Give the extent of all Plasmodium falciparum-infected red blood cells.
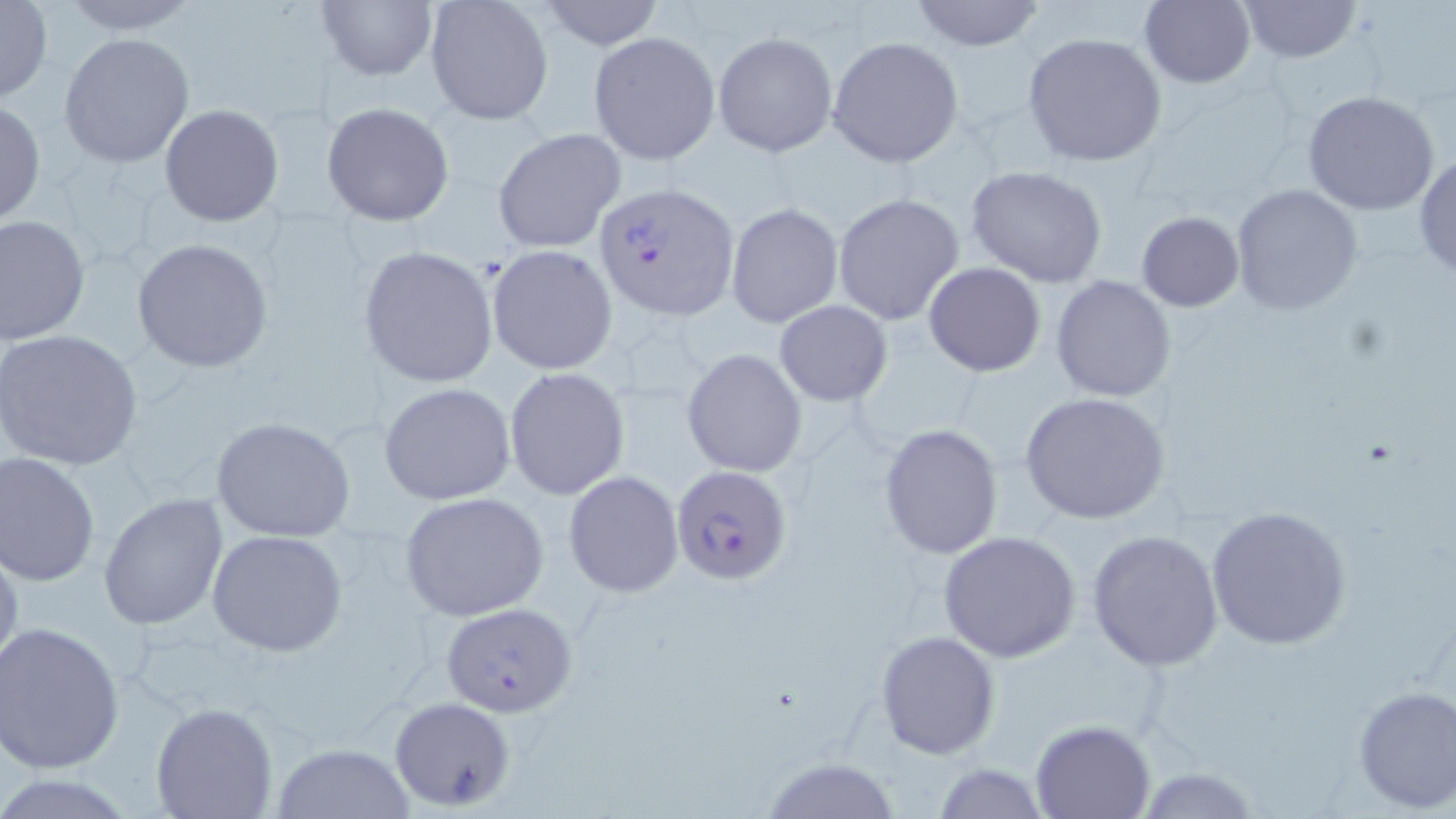

Approximate bounding boxes as [x1, y1, x2, y2] in pixels.
Plasmodium falciparum-infected red blood cells: [593, 182, 740, 321], [672, 465, 794, 586].

slide-level diagnosis = Plasmodium falciparum
preparation = thin blood smear
magnification = 1000x
field of view = single
uninfected red blood cell locations = approximate bounding boxes as [x1, y1, x2, y2] in pixels: [55, 0, 203, 35], [425, 0, 554, 126], [537, 0, 665, 50], [908, 0, 1047, 50], [1140, 0, 1255, 88], [0, 1, 52, 104], [316, 1, 438, 82], [1240, 1, 1360, 63], [712, 30, 838, 158], [588, 31, 722, 165], [1021, 32, 1168, 167], [58, 33, 195, 168], [827, 36, 964, 168], [1301, 90, 1440, 215], [0, 100, 46, 227], [321, 101, 456, 226], [159, 103, 285, 227], [493, 128, 627, 252], [1414, 153, 1456, 278], [965, 165, 1108, 287], [1230, 184, 1362, 315], [832, 194, 965, 325], [726, 202, 843, 328], [1135, 211, 1242, 312], [1, 215, 91, 345], [131, 237, 274, 373], [487, 244, 618, 376], [358, 245, 498, 388], [923, 261, 1047, 378], [1051, 274, 1176, 402], [774, 301, 893, 406], [0, 329, 144, 470], [683, 348, 807, 476], [505, 368, 632, 501], [378, 382, 516, 505], [1021, 391, 1171, 525], [212, 416, 356, 542], [878, 423, 1004, 560], [0, 451, 101, 586], [563, 471, 684, 597], [99, 493, 230, 631], [399, 493, 549, 619], [1205, 504, 1353, 651], [207, 528, 348, 656], [1086, 530, 1224, 669], [937, 531, 1081, 663], [0, 540, 23, 682], [441, 601, 575, 718], [1, 620, 126, 774], [876, 630, 1001, 759], [1352, 683, 1456, 813], [389, 694, 517, 811], [151, 700, 278, 818], [1030, 719, 1156, 818], [272, 745, 416, 818], [758, 756, 907, 818], [930, 762, 1052, 818]
image size = 1456×819 pixels
modality = optical microscopy
stain = May-Grünwald-Giemsa